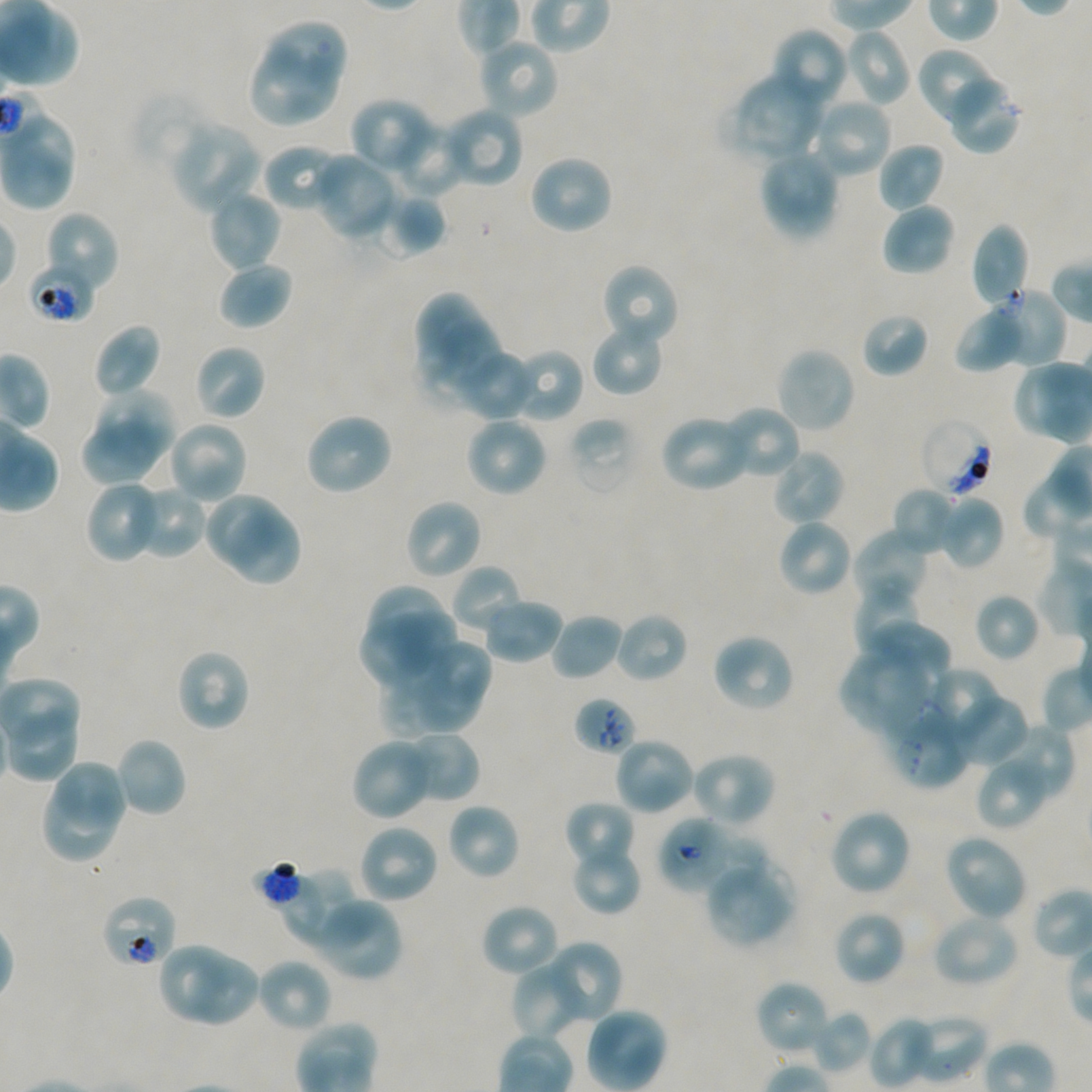
Not every red blood cell is marked. A life-cycle stage — or a range of stages, where the recorded stages span more than one — follows each staged infected red blood cell.
{
  "locations_of_red_blood_cells_of_indeterminate_infection_status": "approximate bounding boxes as (x1, y1, x2, y2) in pixels: (28, 259, 96, 323), (920, 417, 994, 498), (886, 701, 973, 790), (657, 816, 731, 896), (251, 860, 314, 917), (100, 894, 178, 970)",
  "donor_blood_group": "A+/O+",
  "locations_of_uninfected_red_blood_cells": "approximate bounding boxes as (x1, y1, x2, y2) in pixels: (266, 23, 345, 88), (770, 26, 850, 111), (842, 28, 912, 108), (478, 37, 559, 120), (916, 48, 1000, 127), (249, 59, 337, 126), (731, 71, 826, 163), (944, 74, 1021, 154), (131, 90, 213, 172), (812, 96, 894, 179), (350, 97, 438, 175), (441, 107, 524, 188), (1, 114, 73, 179), (390, 120, 467, 198), (170, 121, 262, 215), (877, 142, 945, 212), (262, 145, 348, 213), (4, 149, 75, 212), (758, 149, 840, 242), (312, 151, 398, 240), (528, 153, 614, 236), (206, 188, 282, 273), (374, 192, 446, 259), (881, 202, 955, 277), (43, 211, 120, 297), (970, 221, 1031, 308), (217, 259, 293, 330), (599, 263, 679, 349), (983, 287, 1067, 368), (414, 292, 486, 354), (954, 305, 1025, 372), (861, 312, 928, 378), (591, 321, 665, 397), (432, 322, 500, 392), (93, 323, 162, 399), (194, 343, 268, 421), (774, 346, 856, 433), (509, 348, 583, 422), (462, 354, 536, 422), (92, 388, 178, 467), (720, 406, 802, 481), (304, 412, 393, 496), (80, 413, 168, 486), (660, 413, 753, 492), (464, 415, 548, 498), (568, 417, 636, 497), (166, 420, 249, 505), (769, 448, 846, 526), (85, 481, 162, 563), (129, 484, 207, 560), (892, 486, 959, 557), (204, 491, 278, 565), (938, 495, 1005, 570), (403, 498, 483, 581), (225, 509, 302, 587), (776, 518, 854, 598), (852, 527, 930, 608), (451, 564, 526, 636), (853, 582, 931, 661), (369, 583, 446, 650), (974, 592, 1040, 662), (480, 598, 564, 664), (389, 610, 460, 676), (614, 611, 689, 684), (549, 612, 625, 682), (360, 620, 426, 689), (865, 621, 953, 700), (710, 632, 796, 714), (425, 636, 489, 703), (840, 644, 934, 740), (175, 647, 251, 733), (410, 666, 481, 731), (923, 668, 1003, 744), (381, 674, 447, 735), (951, 693, 1030, 768), (989, 723, 1074, 806), (399, 730, 479, 805), (114, 736, 187, 818), (613, 737, 695, 816), (350, 738, 436, 821), (689, 750, 776, 828), (975, 752, 1052, 831), (58, 761, 126, 833), (40, 782, 115, 864), (563, 800, 636, 872), (446, 802, 521, 881), (828, 808, 913, 897), (358, 823, 440, 905), (942, 833, 1028, 923), (692, 836, 769, 899), (570, 843, 642, 916), (279, 864, 363, 952), (710, 871, 797, 949), (312, 897, 403, 982), (479, 903, 561, 978), (832, 909, 907, 987), (930, 913, 1021, 989), (157, 941, 260, 1027), (544, 941, 622, 1025), (256, 958, 333, 1034), (513, 958, 592, 1040), (756, 979, 831, 1057), (811, 1010, 871, 1073), (907, 1011, 989, 1085), (868, 1015, 937, 1089)",
  "preparation": "thin blood film",
  "culture": "static in-vitro Plasmodium falciparum strain NF54",
  "field_of_view": "one from this slide",
  "stain": "Giemsa",
  "objective": "100x, oil immersion, numerical aperture 1.45",
  "image_size": "1092×1092 pixels",
  "locations_of_infected_red_blood_cells": "approximate bounding boxes as (x1, y1, x2, y2) in pixels: (574, 696, 637, 756) late ring"
}